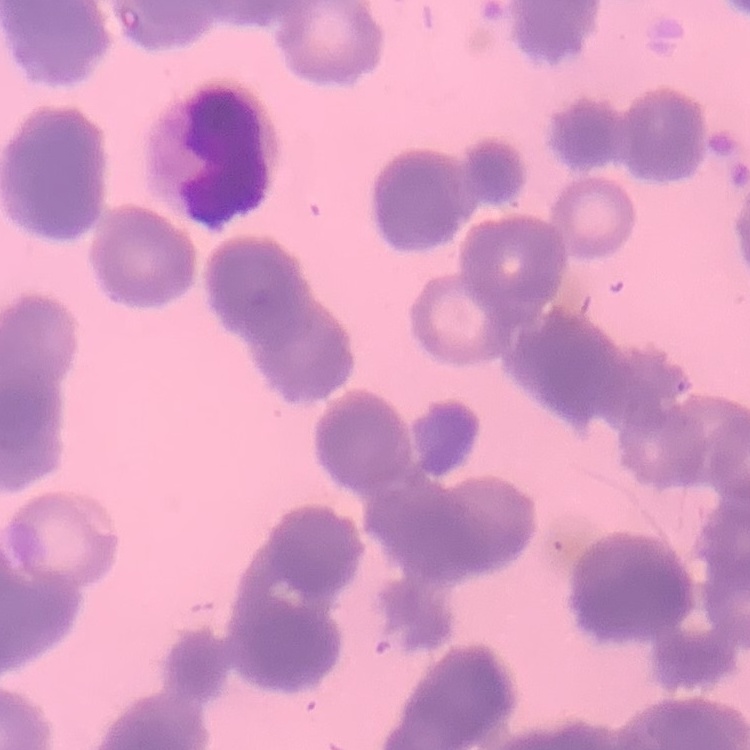
Summary:
  - Erythrocyte morphology: rouleaux formation
  - Stain: Field's or Giemsa
  - Preparation: thin blood smear
  - Image type: square crop of a larger photomicrograph